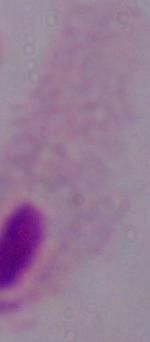
Summary:
  - Identification: trichomonad
  - Magnification: 1000x
  - Modality: micrograph